Assess this cell for malaria.
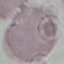
It is uninfected.

Summary:
  - Image type: automatically extracted cell patch, resized to 64 × 64 pixels
  - Preparation: thin blood smear
  - Capture: smartphone camera at the microscope eyepiece
  - Stain: Giemsa